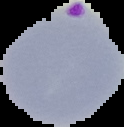

Summary:
  - Preparation: thin blood smear
  - Image size: 124×127 pixels
  - Result: Plasmodium parasites detected
  - Image type: segmented cell region on a black background